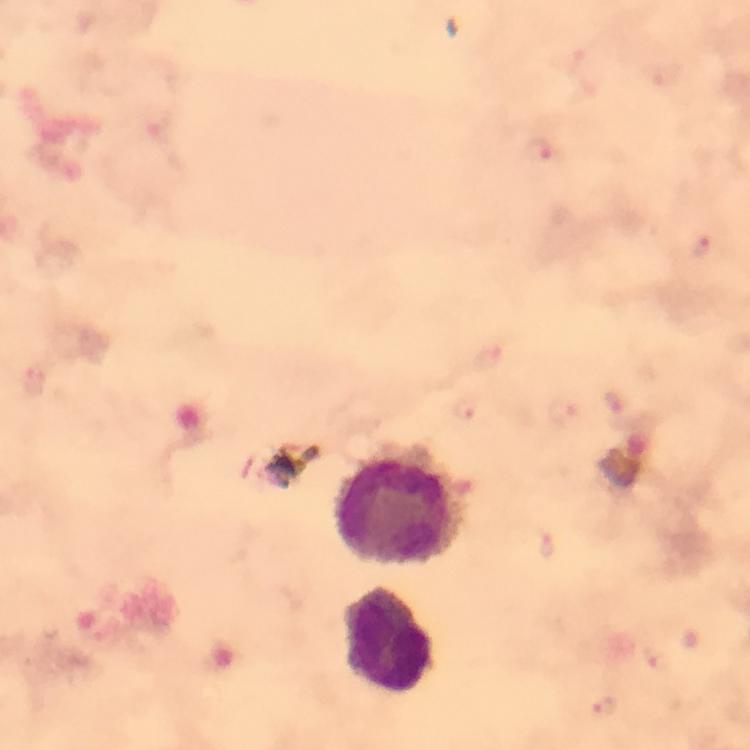
Approximate centers as {x, y} in pixels.
Summary:
  - Plasmodium parasite locations: {539, 152}, {703, 246}, {490, 358}, {36, 382}, {468, 410}, {656, 661}, {603, 709}
  - Leukocyte locations: {401, 506}, {389, 641}
  - Stain: Giemsa
  - Immersion oil: used
  - Capture: smartphone camera through the microscope
  - Magnification: 100x
  - Context: from a diagnostic examination for malaria
  - Image size: 750×750 pixels
  - Preparation: thick blood smear
  - Cropped from: one field of view